Classify this cell by malaria status.
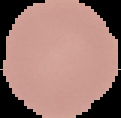

It is uninfected.

Summary:
  - Image size: 121×118 pixels
  - Preparation: thin blood smear
  - Image type: cell region segmented out of the field of view; surrounding area masked to black